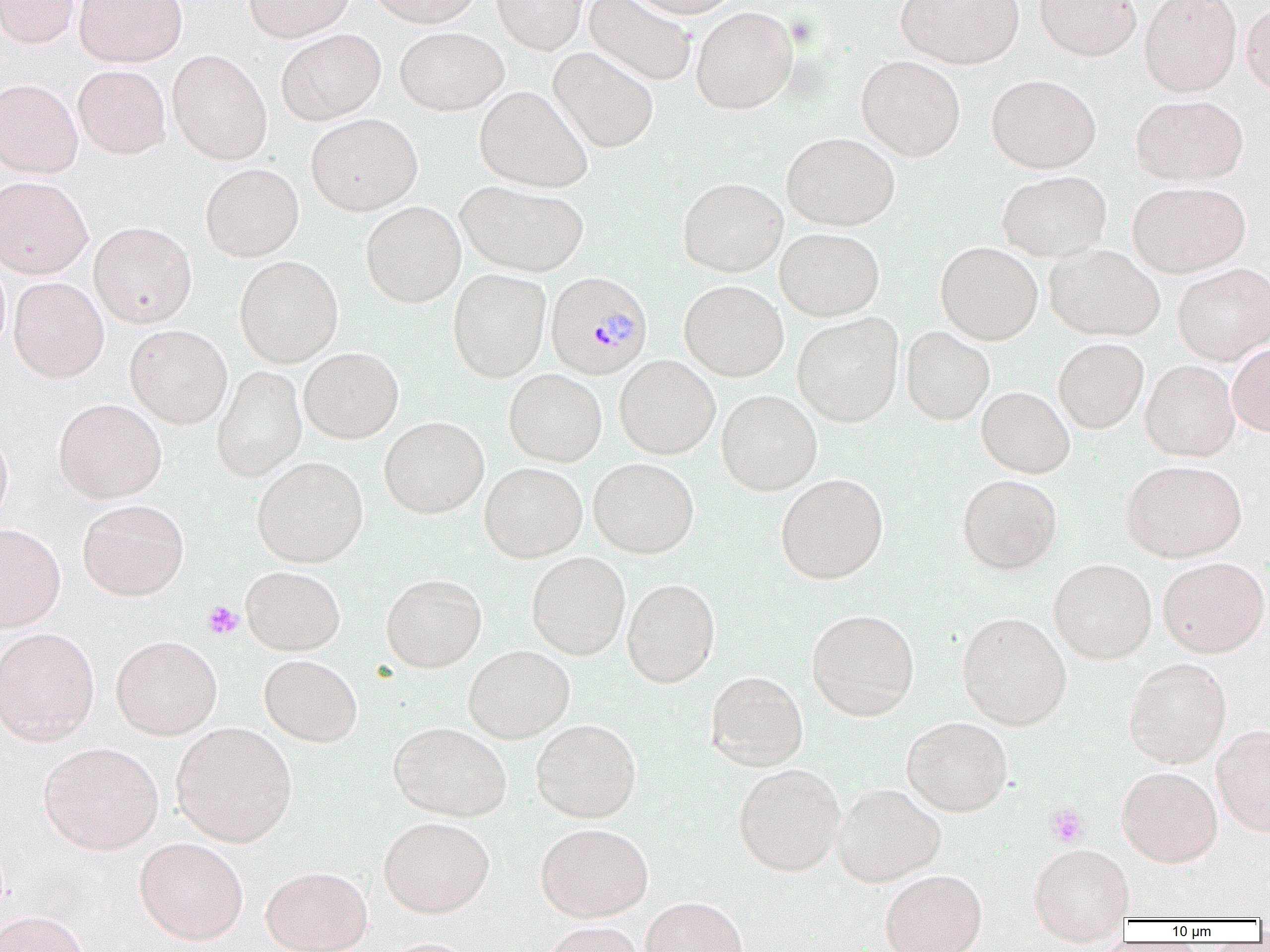
Summary:
  - Coordinate format: approximate bounding boxes as (x1, y1, x2, y2) in pixels
  - Plasmodium malariae-infected red blood cell locations: (545, 271, 652, 380)
  - Uninfected red blood cell locations: (0, 0, 80, 48), (73, 0, 187, 67), (244, 0, 354, 42), (367, 0, 483, 28), (493, 0, 587, 54), (584, 0, 696, 86), (627, 0, 741, 18), (896, 0, 1023, 68), (1034, 0, 1142, 61), (1139, 0, 1242, 97), (1241, 1, 1270, 98), (691, 6, 798, 114), (395, 27, 508, 115), (276, 29, 385, 125), (548, 47, 659, 153), (167, 50, 272, 165), (856, 56, 965, 161), (73, 65, 171, 159), (986, 74, 1101, 173), (0, 78, 83, 178), (474, 85, 592, 192), (1131, 94, 1248, 186), (306, 113, 422, 215), (782, 132, 899, 231), (200, 163, 304, 261), (997, 170, 1111, 261), (0, 175, 93, 279), (678, 177, 787, 278), (456, 180, 589, 277), (1127, 181, 1250, 277), (360, 201, 466, 307), (88, 221, 197, 328), (775, 227, 885, 322), (936, 242, 1043, 345), (1045, 243, 1165, 341), (234, 255, 343, 368), (0, 256, 11, 358), (1172, 262, 1270, 365), (448, 268, 551, 382), (9, 277, 109, 383), (679, 280, 788, 381), (792, 313, 904, 427), (125, 324, 232, 428), (901, 326, 994, 425), (1053, 338, 1148, 433), (1227, 343, 1270, 437), (299, 347, 403, 444), (614, 355, 720, 459), (1140, 361, 1240, 461), (212, 366, 307, 482), (503, 369, 607, 466), (976, 386, 1074, 478), (716, 390, 823, 495), (53, 398, 167, 503), (379, 416, 489, 518), (0, 426, 13, 528), (252, 456, 369, 567), (588, 457, 699, 558), (1121, 459, 1246, 561), (479, 462, 587, 563), (775, 472, 888, 584), (957, 474, 1062, 574), (77, 499, 189, 601), (0, 523, 65, 632), (527, 551, 630, 659), (1158, 556, 1269, 658), (1048, 558, 1157, 664), (240, 565, 346, 655), (381, 573, 487, 672), (622, 578, 720, 688), (806, 608, 920, 721), (957, 611, 1072, 730), (0, 627, 100, 746), (111, 634, 222, 739), (463, 645, 575, 743), (259, 654, 363, 747), (1124, 657, 1231, 768), (705, 670, 808, 771), (902, 716, 1013, 816), (530, 718, 642, 823), (171, 722, 297, 847), (388, 722, 512, 821), (1212, 724, 1270, 836), (38, 741, 163, 854), (733, 763, 845, 876), (1116, 767, 1222, 866), (832, 783, 946, 887), (378, 816, 495, 918), (535, 822, 653, 921), (134, 837, 249, 945), (1027, 842, 1134, 935), (260, 865, 373, 952), (880, 870, 987, 952), (640, 896, 749, 952), (0, 909, 88, 952), (541, 921, 647, 952), (371, 937, 482, 952)
  - Platelet locations: (202, 601, 242, 640), (1045, 803, 1089, 847)
  - Slide-level diagnosis: Plasmodium malariae
  - Magnification: 1000x
  - Field of view: one of a larger specimen
  - Modality: light microscopy
  - Image size: 1270×952 pixels
  - Preparation: thin blood smear